Report the malaria status of this cell.
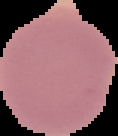

Uninfected.

Summary:
  - Image type: segmented cell region with the area outside set to black
  - Preparation: thin blood smear
  - Image size: 118×136 pixels